Look for Plasmodium parasites.
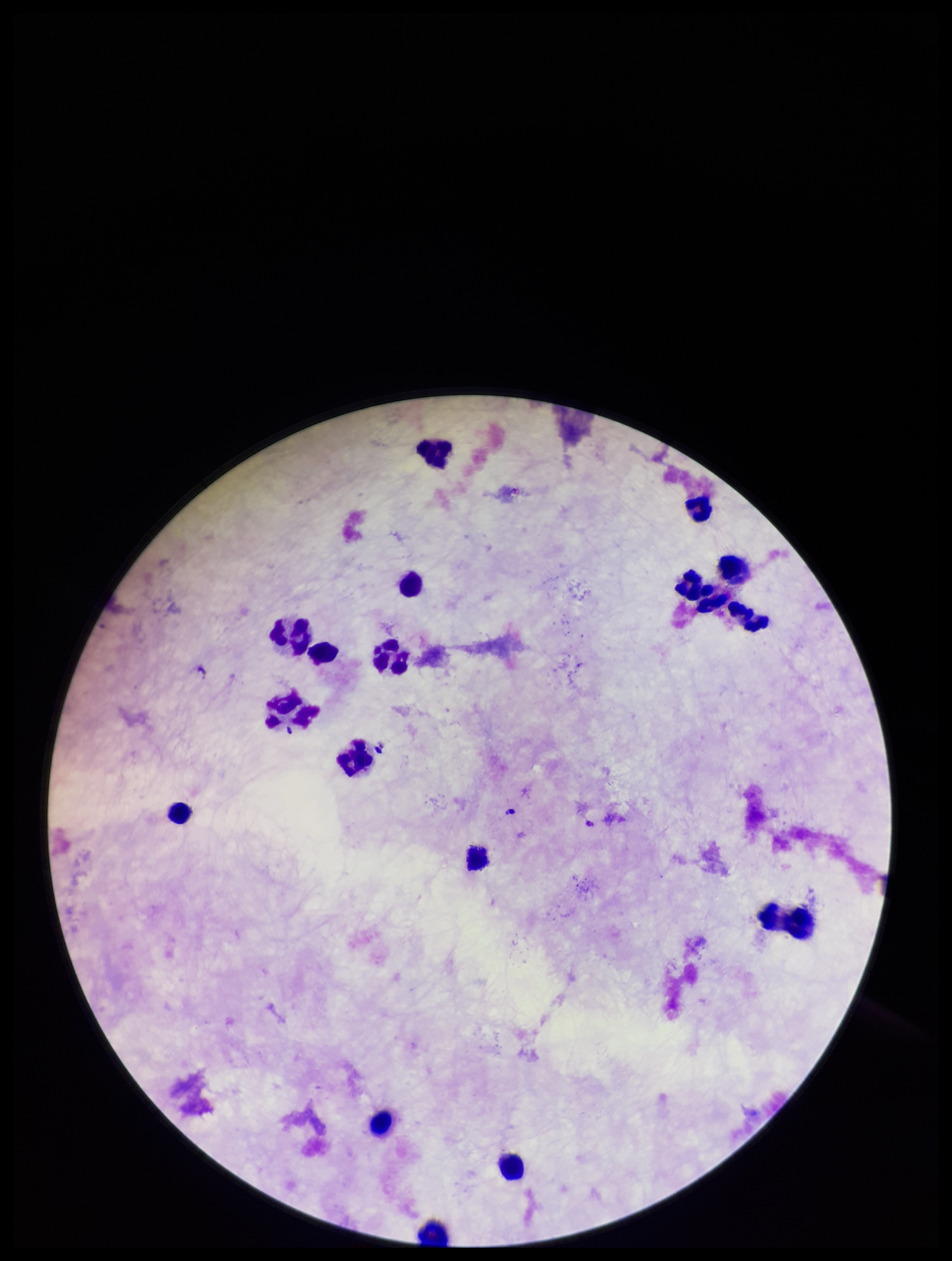
None identified.

Stained with Giemsa. Preparation: thick smear. Photographed through the microscope eyepiece with a smartphone camera. Patient malaria status: negative. Image is 952×1261 pixels. Parasite count: 0. Leukocyte count: 18. One field from this slide.